Assess this cell for malaria.
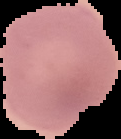

It is uninfected.

{
  "preparation": "thin blood film",
  "image_type": "cell region segmented out of the field of view; surrounding area masked to black",
  "image_size": "121×139 pixels"
}